Classify this cell by malaria status.
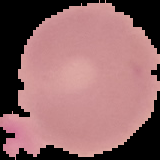

Uninfected.

image size = 160×160 pixels
image type = segmented cell region on a black background
preparation = thin blood film